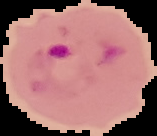
Image is 157×136 pixels. From a thin blood smear. Result: Plasmodium parasites identified. Segmented cell region on a black background.